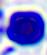

magnification = 400x
identification = leukocyte
modality = micrograph